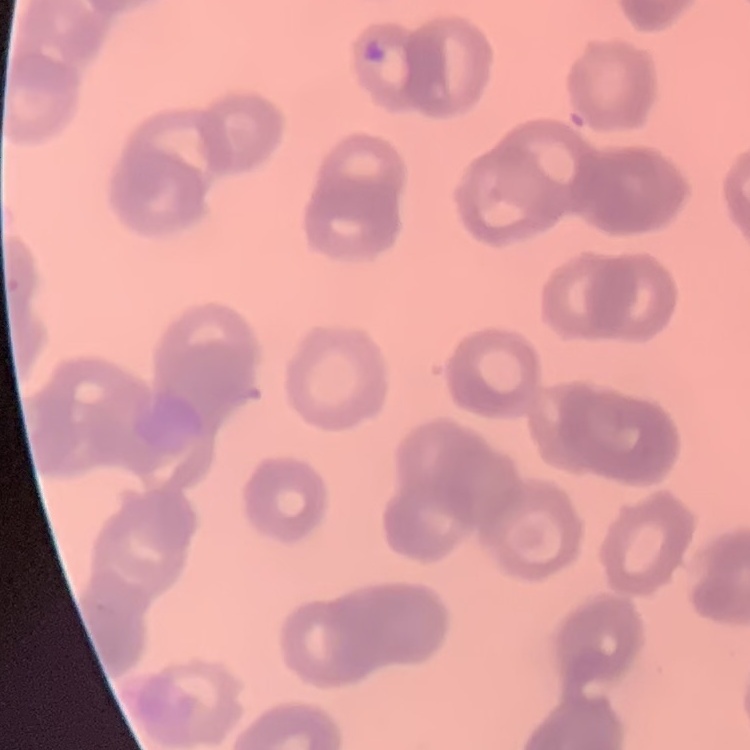
erythrocyte_morphology: rouleaux formation
image_type: square crop of a larger photomicrograph
stain: Field's or Giemsa
preparation: thin blood smear